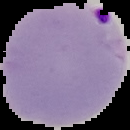
image size = 130×130 pixels
malaria status = parasitized
preparation = thin blood smear
image type = segmented cell region on a black background